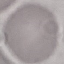

Malaria status: uninfected. Giemsa-stained preparation. Acquired by smartphone through the microscope eyepiece. Automatically extracted cell patch, resized to 64 × 64 pixels. Thin blood smear.